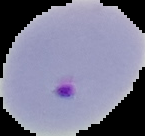

Summary:
  - Image size: 145×136 pixels
  - Image type: segmented cell region with the area outside set to black
  - Result: Plasmodium parasites detected
  - Preparation: thin blood film